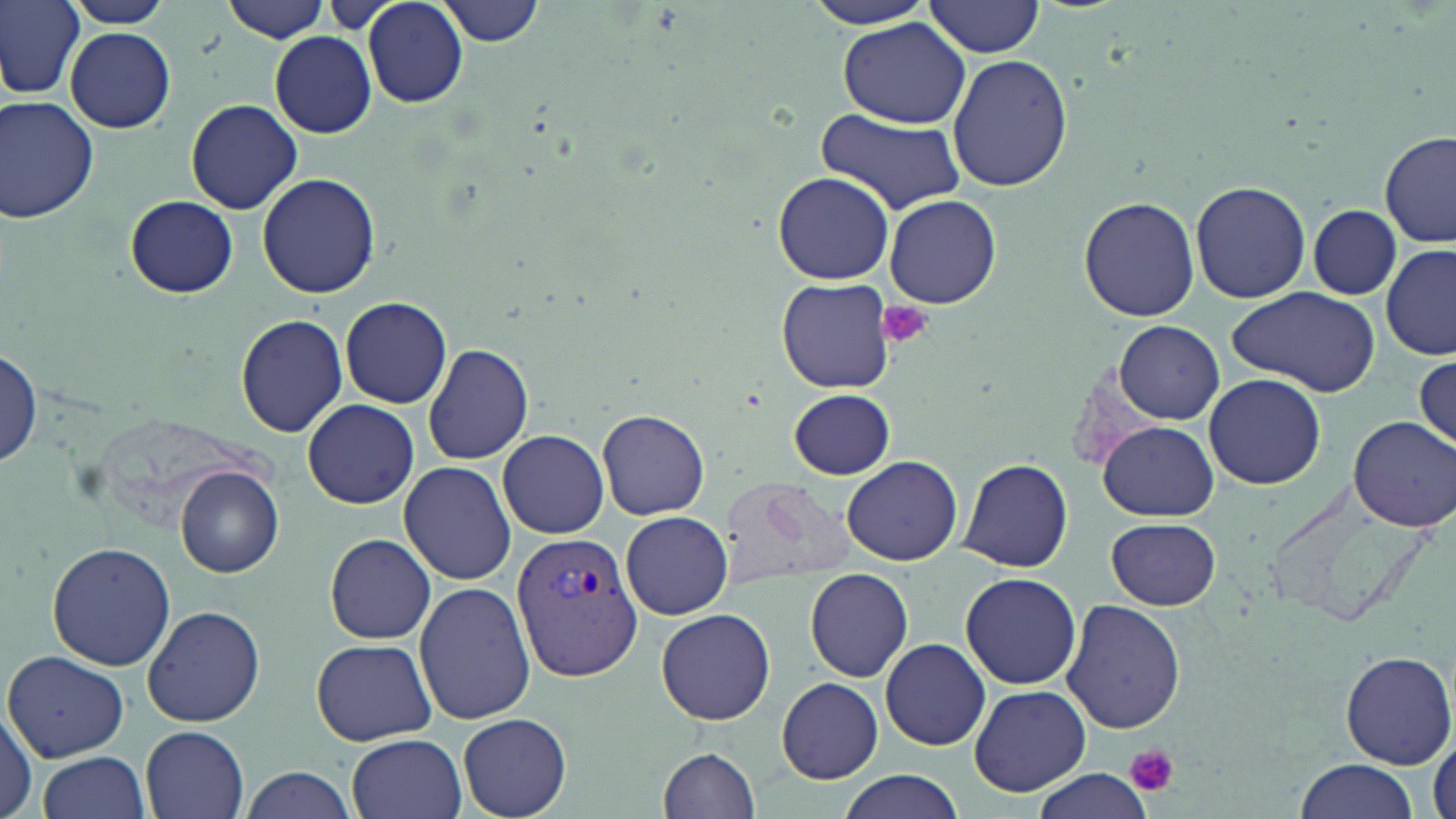
slide-level diagnosis = Plasmodium vivax
image size = 1456×819 pixels
magnification = 1000x
stain = May-Grünwald-Giemsa
modality = light microscopy
field of view = single
uninfected red blood cell locations = approximate bounding boxes as named x1/y1/x2/y2 corners in pixels: (x1=1, y1=0, x2=84, y2=99), (x1=66, y1=0, x2=173, y2=28), (x1=363, y1=0, x2=469, y2=107), (x1=438, y1=0, x2=546, y2=45), (x1=219, y1=1, x2=332, y2=44), (x1=798, y1=1, x2=941, y2=28), (x1=924, y1=2, x2=1049, y2=59), (x1=839, y1=19, x2=971, y2=129), (x1=65, y1=27, x2=176, y2=133), (x1=270, y1=32, x2=376, y2=137), (x1=947, y1=54, x2=1073, y2=192), (x1=0, y1=97, x2=100, y2=224), (x1=186, y1=99, x2=301, y2=213), (x1=812, y1=109, x2=965, y2=216), (x1=1378, y1=131, x2=1454, y2=246), (x1=772, y1=172, x2=895, y2=283), (x1=257, y1=174, x2=379, y2=297), (x1=1190, y1=179, x2=1311, y2=303), (x1=885, y1=194, x2=1001, y2=309), (x1=126, y1=195, x2=238, y2=299), (x1=1079, y1=196, x2=1200, y2=320), (x1=1307, y1=204, x2=1400, y2=301), (x1=1381, y1=244, x2=1456, y2=363), (x1=776, y1=279, x2=895, y2=393), (x1=1227, y1=287, x2=1380, y2=395), (x1=339, y1=295, x2=452, y2=408), (x1=234, y1=313, x2=350, y2=438), (x1=1115, y1=320, x2=1224, y2=422), (x1=1, y1=343, x2=42, y2=472), (x1=423, y1=343, x2=534, y2=465), (x1=1413, y1=353, x2=1455, y2=453), (x1=1203, y1=374, x2=1328, y2=491), (x1=788, y1=388, x2=895, y2=480), (x1=302, y1=398, x2=419, y2=509), (x1=598, y1=409, x2=711, y2=520), (x1=1348, y1=416, x2=1456, y2=532), (x1=1098, y1=420, x2=1217, y2=522), (x1=497, y1=429, x2=609, y2=538), (x1=842, y1=456, x2=962, y2=566), (x1=958, y1=458, x2=1073, y2=573), (x1=398, y1=461, x2=516, y2=585), (x1=174, y1=466, x2=284, y2=578), (x1=715, y1=477, x2=862, y2=589), (x1=622, y1=511, x2=733, y2=620), (x1=1106, y1=517, x2=1221, y2=610), (x1=325, y1=535, x2=436, y2=643), (x1=47, y1=541, x2=176, y2=671), (x1=805, y1=568, x2=914, y2=682), (x1=959, y1=572, x2=1082, y2=689), (x1=414, y1=581, x2=537, y2=727), (x1=1061, y1=600, x2=1185, y2=734), (x1=144, y1=604, x2=265, y2=727), (x1=657, y1=607, x2=776, y2=725), (x1=312, y1=638, x2=437, y2=746), (x1=880, y1=638, x2=990, y2=751), (x1=1340, y1=650, x2=1455, y2=768), (x1=5, y1=652, x2=128, y2=760), (x1=777, y1=677, x2=883, y2=783), (x1=968, y1=684, x2=1093, y2=797), (x1=0, y1=706, x2=39, y2=819), (x1=459, y1=712, x2=572, y2=818), (x1=141, y1=725, x2=250, y2=819), (x1=347, y1=734, x2=465, y2=819), (x1=657, y1=746, x2=761, y2=819), (x1=37, y1=751, x2=151, y2=819), (x1=1296, y1=758, x2=1418, y2=818), (x1=241, y1=766, x2=357, y2=819), (x1=1027, y1=766, x2=1160, y2=819), (x1=836, y1=772, x2=970, y2=819)
platelet locations = approximate bounding boxes as named x1/y1/x2/y2 corners in pixels: (x1=879, y1=301, x2=932, y2=348), (x1=1127, y1=743, x2=1179, y2=795)
preparation = thin blood film
Plasmodium vivax-infected red blood cell locations = approximate bounding boxes as named x1/y1/x2/y2 corners in pixels: (x1=512, y1=529, x2=645, y2=684)